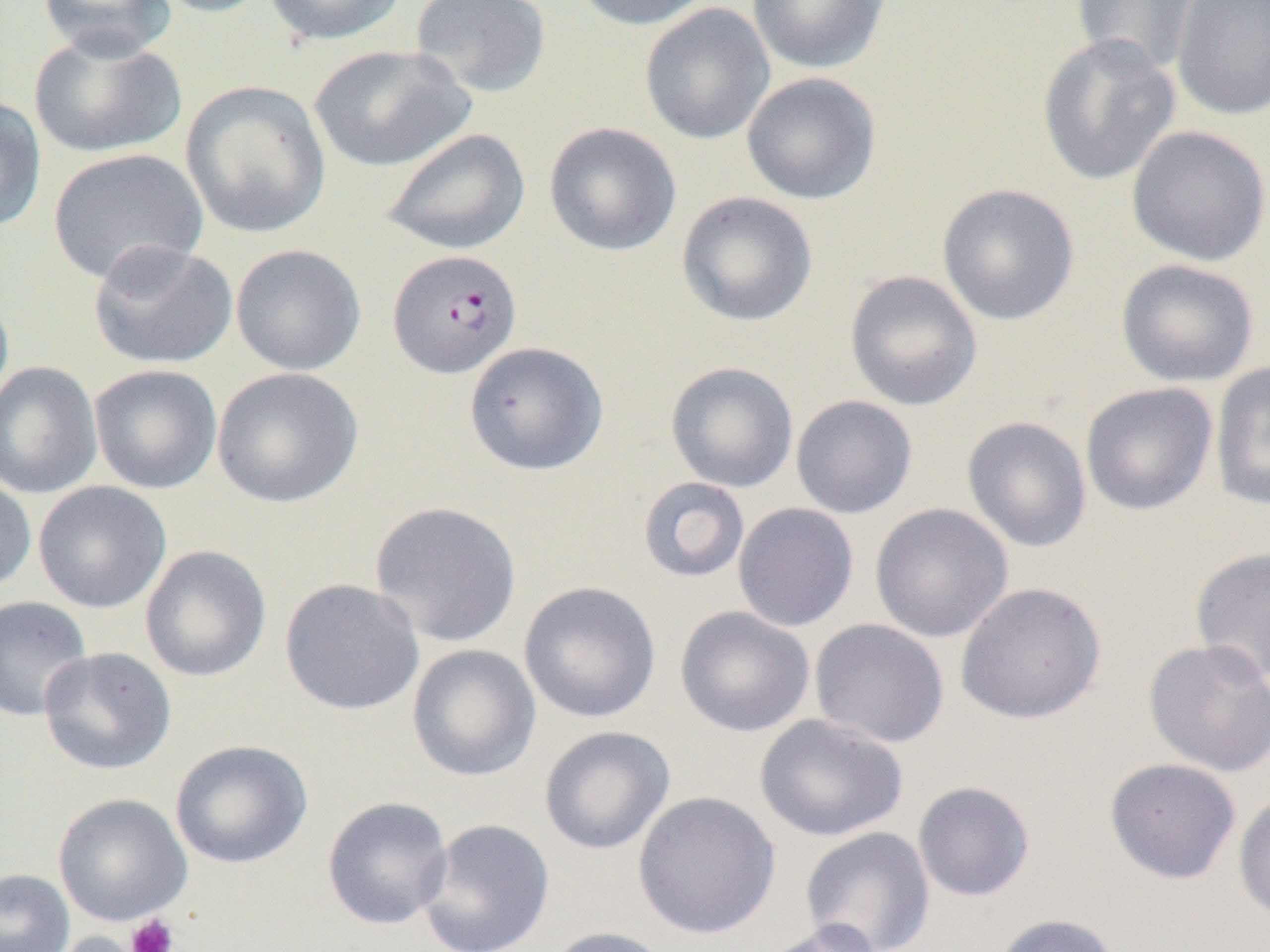

slide_level_diagnosis: Plasmodium falciparum
magnification: 1000x
image_size: 1270×952 pixels
preparation: thin blood film
platelet_locations: 'approximate bounding boxes as [x1, y1, x2, y2] in pixels: [125, 913, 179, 952]'
field_of_view: one of a larger specimen
plasmodium_falciparum_infected_red_blood_cell_locations: 'approximate bounding boxes as [x1, y1, x2, y2] in pixels: [387, 248, 523, 379]'
modality: light microscopy
uninfected_red_blood_cell_locations: 'approximate bounding boxes as [x1, y1, x2, y2] in pixels: [38, 0, 176, 60], [146, 0, 276, 18], [263, 0, 407, 46], [410, 0, 551, 98], [572, 0, 719, 30], [747, 0, 891, 74], [1072, 0, 1200, 77], [1171, 0, 1270, 121], [639, 3, 775, 145], [29, 30, 187, 159], [1036, 34, 1181, 186], [308, 44, 474, 172], [741, 72, 881, 205], [180, 81, 332, 239], [0, 96, 47, 234], [543, 122, 681, 256], [1126, 125, 1270, 266], [378, 127, 531, 255], [47, 147, 209, 286], [937, 183, 1080, 326], [676, 191, 818, 327], [87, 240, 238, 370], [231, 244, 366, 376], [1116, 259, 1259, 387], [844, 270, 983, 411], [0, 290, 14, 417], [463, 341, 608, 477], [1209, 360, 1270, 511], [0, 361, 103, 499], [665, 361, 799, 493], [88, 363, 223, 495], [211, 367, 364, 509], [1080, 382, 1218, 515], [791, 395, 917, 519], [962, 416, 1092, 552], [0, 470, 37, 597], [637, 476, 750, 584], [32, 481, 171, 613], [369, 501, 522, 648], [733, 502, 859, 632], [869, 503, 1013, 643], [140, 545, 272, 682], [1190, 546, 1270, 686], [279, 578, 425, 715], [519, 581, 661, 723], [954, 581, 1106, 725], [0, 595, 93, 722], [675, 606, 815, 737], [810, 618, 949, 749], [1142, 638, 1270, 777], [407, 644, 541, 782], [38, 647, 176, 775], [754, 713, 908, 842], [539, 725, 675, 855], [170, 739, 312, 869], [1104, 757, 1241, 885], [912, 781, 1035, 901], [1233, 789, 1270, 922], [633, 790, 780, 939], [53, 792, 192, 927], [321, 796, 453, 930], [417, 818, 555, 952], [800, 827, 935, 952], [0, 869, 75, 952], [990, 913, 1122, 952], [757, 920, 888, 952], [543, 926, 677, 952], [33, 930, 151, 952]'